Name the blood parasite species.
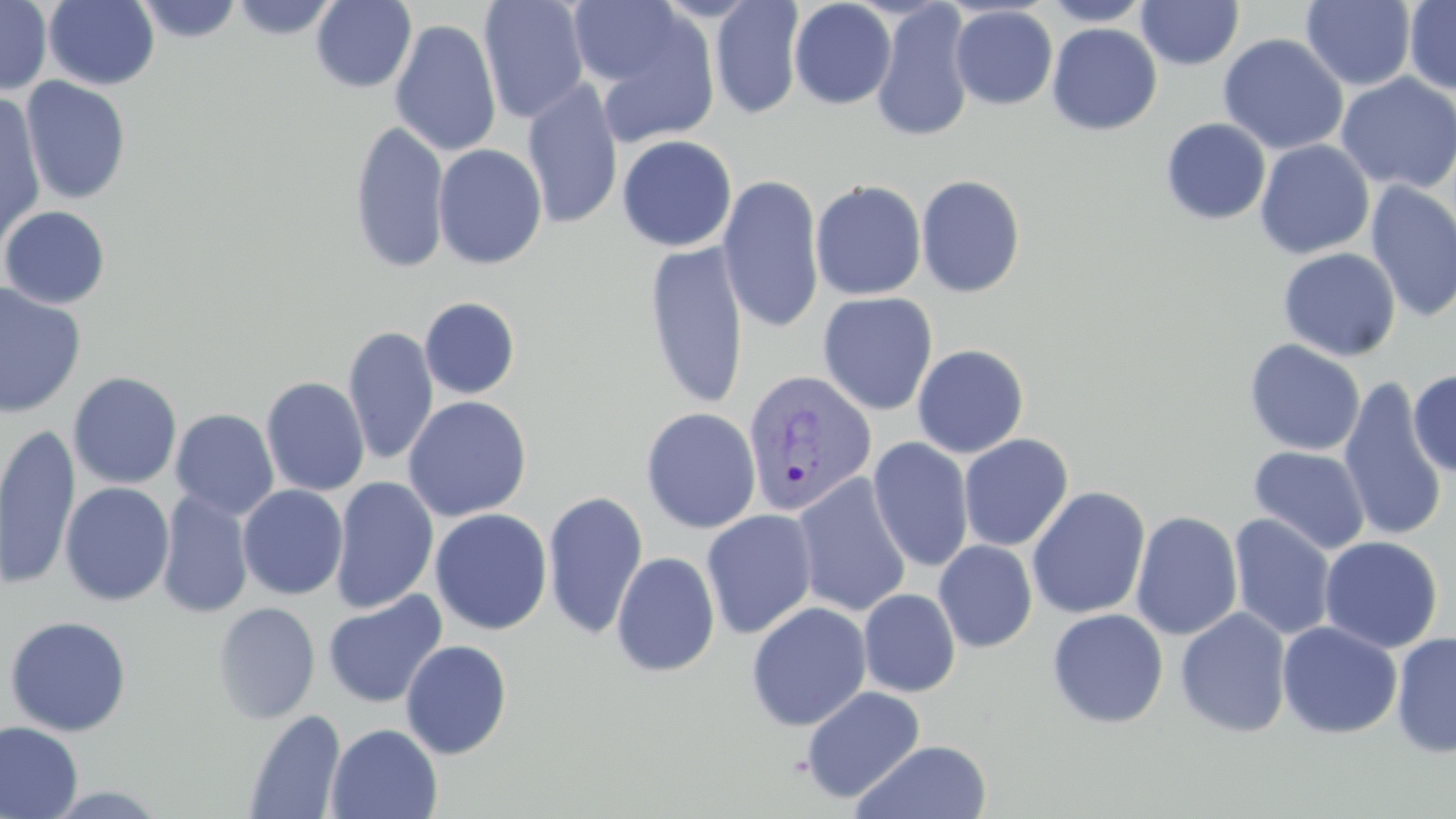

Plasmodium vivax.

Approximate bounding boxes as (x1,y1)-(x2,y2) corner pairs in pixels. Uninfected red blood cell locations: (44,0)-(160,90), (133,0)-(243,43), (229,0)-(340,40), (310,0)-(417,93), (478,0)-(590,124), (1040,0)-(1153,26), (1136,0)-(1244,70), (1404,0)-(1456,95), (0,1)-(52,95), (711,1)-(805,119), (789,1)-(897,109), (1300,1)-(1417,91), (870,2)-(975,143), (577,3)-(721,141), (950,5)-(1058,110), (389,18)-(502,157), (1046,23)-(1162,135), (1218,33)-(1348,155), (1335,73)-(1456,194), (20,77)-(132,205), (522,79)-(623,230), (0,97)-(46,246), (1160,117)-(1271,225), (349,120)-(451,274), (617,134)-(737,252), (1255,140)-(1375,259), (432,143)-(548,270), (717,174)-(825,334), (915,174)-(1026,298), (810,179)-(927,300), (1364,180)-(1456,323), (0,205)-(111,310), (644,241)-(749,411), (1277,247)-(1401,361), (0,282)-(87,419), (817,292)-(938,415), (419,297)-(520,400), (343,325)-(438,467), (1244,339)-(1366,456), (912,344)-(1029,458), (1408,370)-(1455,478), (68,371)-(183,490), (260,376)-(370,497), (1337,376)-(1449,542), (403,396)-(532,522), (640,407)-(761,534), (170,408)-(279,520), (0,423)-(80,591), (958,434)-(1074,552), (868,437)-(974,573), (1248,445)-(1371,556), (792,473)-(912,618), (330,476)-(439,614), (60,481)-(175,606), (238,484)-(348,600), (1026,486)-(1151,620), (157,490)-(253,618), (543,490)-(648,640), (429,508)-(552,635), (700,509)-(819,639), (1130,510)-(1243,641), (1228,513)-(1336,641), (1319,535)-(1443,654), (933,540)-(1038,653), (611,551)-(720,677), (859,588)-(961,697), (322,590)-(447,708), (212,601)-(321,724), (746,601)-(872,731), (1175,607)-(1292,738), (1047,608)-(1169,728), (3,615)-(132,737), (1276,620)-(1403,739), (1391,631)-(1456,759), (400,639)-(513,759), (801,685)-(926,804), (244,709)-(346,818), (0,721)-(83,819), (326,723)-(443,819), (851,739)-(994,819). Plasmodium vivax-infected red blood cell locations: (741,369)-(878,517). Optical microscopy. One field of a larger specimen. May-Grünwald-Giemsa-stained preparation. Captured at 1000x magnification. Image is 1456×819 pixels. Thin blood film.